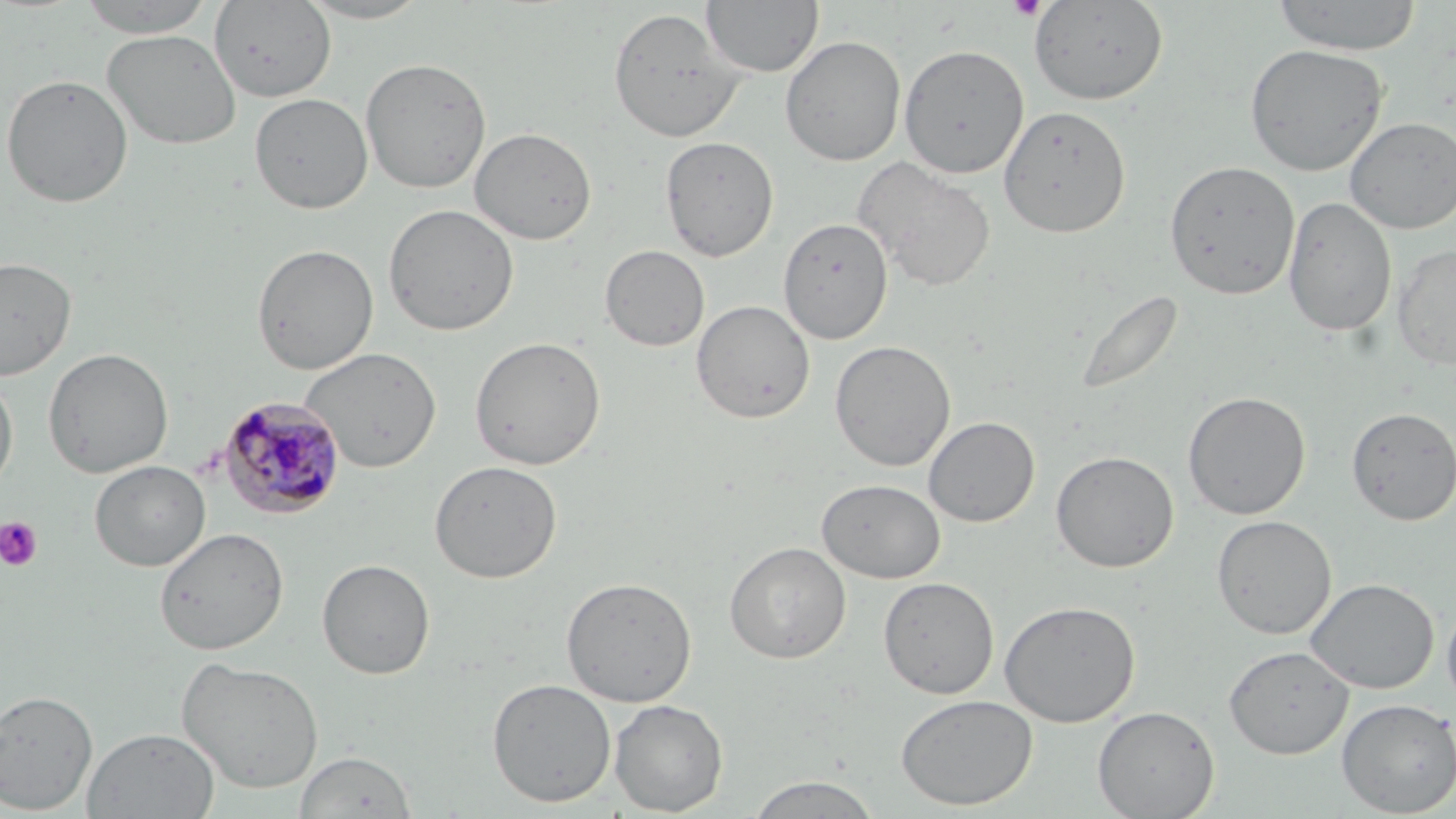

slide_level_diagnosis: Plasmodium malariae
preparation: thin blood film
field_of_view: single
modality: optical microscopy
uninfected_red_blood_cell_locations: 'approximate bounding boxes as (x1,y1)-(x2,y2) corner pairs in pixels: (74,0)-(220,37), (295,0)-(438,24), (702,0)-(824,77), (1271,0)-(1424,55), (210,1)-(337,102), (1028,1)-(1169,106), (607,8)-(746,143), (101,29)-(242,150), (780,35)-(906,166), (1244,43)-(1390,177), (898,44)-(1029,179), (360,57)-(492,193), (0,74)-(134,208), (249,93)-(373,214), (998,104)-(1131,238), (1344,116)-(1456,233), (470,127)-(597,245), (660,135)-(778,261), (852,156)-(997,293), (1164,159)-(1301,300), (1283,196)-(1397,336), (383,203)-(519,336), (778,217)-(893,344), (251,243)-(379,374), (1392,243)-(1456,370), (599,244)-(709,352), (0,256)-(77,380), (1078,288)-(1183,398), (691,299)-(815,424), (469,335)-(606,471), (829,340)-(956,472), (299,347)-(442,473), (42,348)-(174,478), (0,373)-(18,498), (1182,390)-(1311,520), (1346,406)-(1456,525), (923,416)-(1040,527), (1051,450)-(1179,573), (89,460)-(210,571), (428,460)-(563,584), (816,479)-(946,583), (1211,514)-(1337,639), (154,527)-(289,655), (724,541)-(851,664), (317,558)-(435,679), (561,576)-(697,707), (878,577)-(999,699), (1305,578)-(1439,694), (1441,598)-(1456,713), (999,600)-(1140,727), (1223,646)-(1353,759), (176,656)-(325,793), (487,678)-(617,807), (0,688)-(98,814), (895,694)-(1038,810), (609,698)-(728,816), (1336,698)-(1455,816), (1093,705)-(1220,818), (83,727)-(220,818), (294,750)-(418,818), (744,774)-(883,818)'
magnification: 1000x
stain: May-Grünwald-Giemsa
platelet_locations: 'approximate bounding boxes as (x1,y1)-(x2,y2) corner pairs in pixels: (1007,0)-(1047,20), (0,516)-(43,572)'
image_size: 1456×819 pixels
plasmodium_malariae_infected_red_blood_cell_locations: 'approximate bounding boxes as (x1,y1)-(x2,y2) corner pairs in pixels: (217,395)-(345,520)'